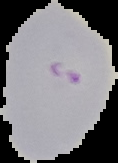 From a thin blood smear. Malaria status: parasitized. Image is 118×163 pixels. Cell region segmented out of the field of view; the surrounding area is masked to black.